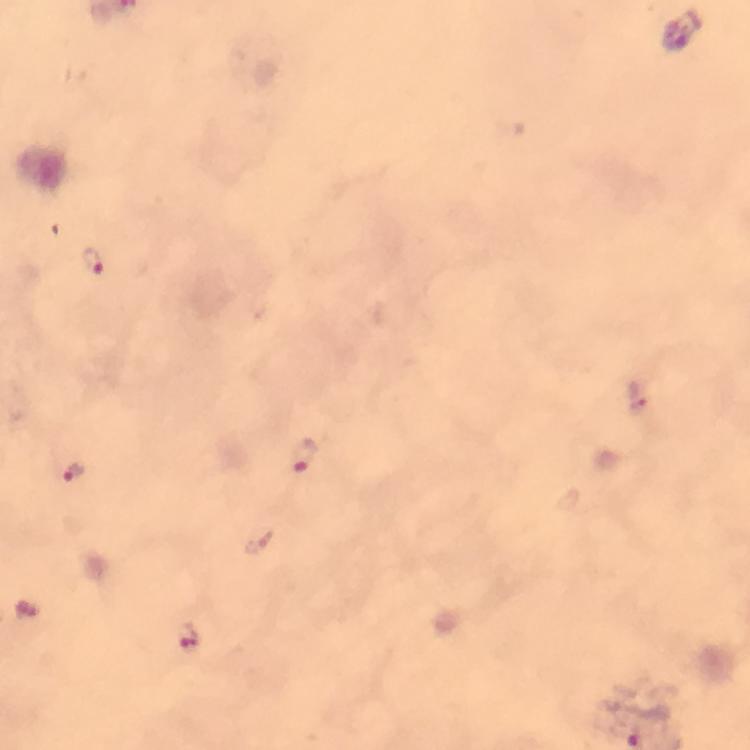

{
  "stain": "Giemsa",
  "plasmodium_parasite_locations": "approximate centers as {x, y} in pixels: {92, 262}, {637, 395}, {304, 457}, {74, 475}, {189, 637}",
  "preparation": "thick smear",
  "cropped_from": "one field of view",
  "magnification": "100x",
  "image_size": "750×750 pixels",
  "capture": "smartphone camera through the microscope",
  "context": "from a malaria diagnostic workup",
  "immersion_oil": "used"
}